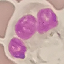 Malaria status: uninfected. Photographed with a smartphone camera at the microscope eyepiece. Giemsa stain. Cell patch, automatically extracted from a larger field of view and resized to 64 × 64 pixels. Thin blood film.